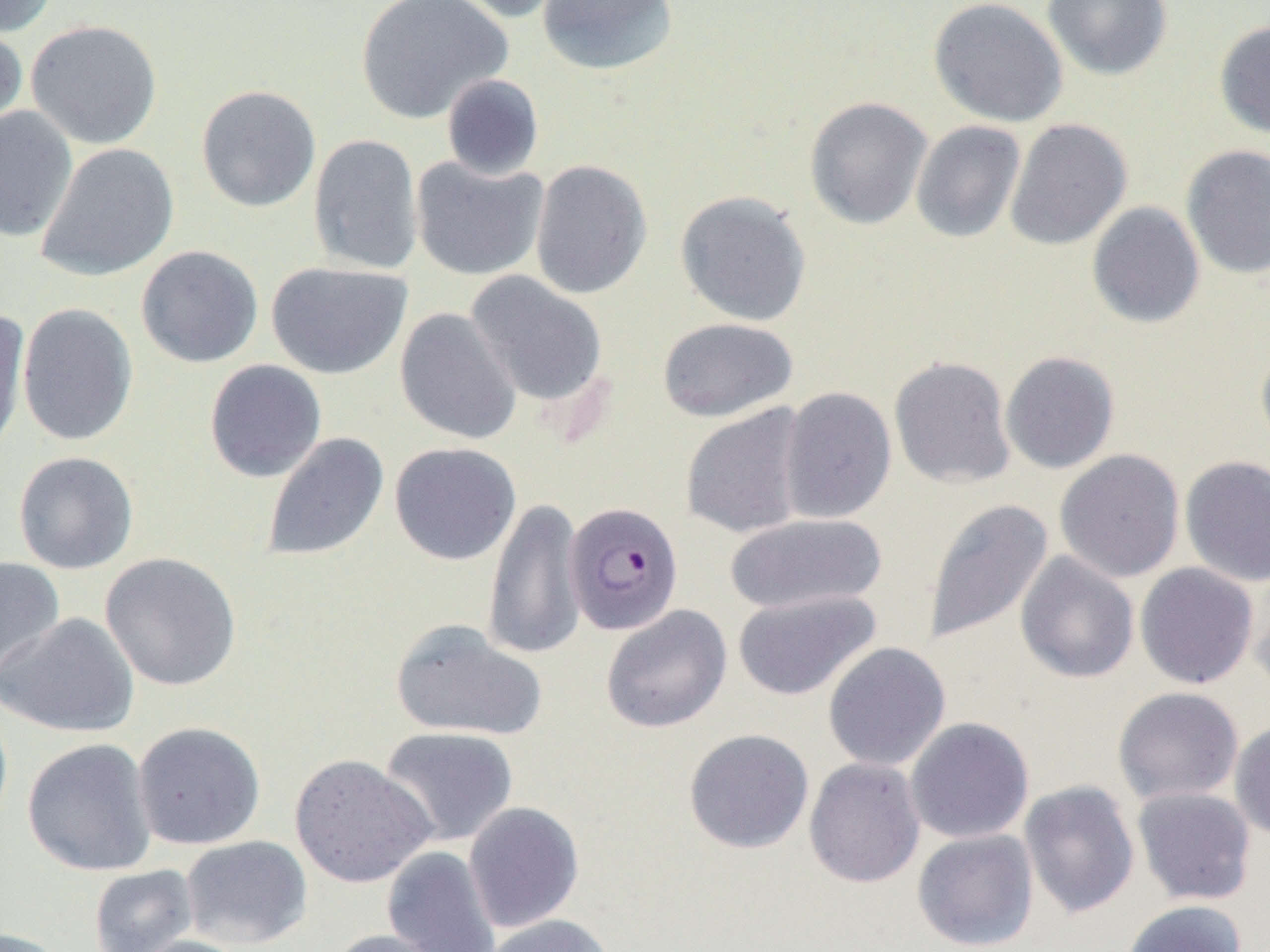

Summary:
  - Coordinate format: approximate bounding boxes as (x1,y1)-(x2,y2) corner pairs in pixels
  - Plasmodium falciparum-infected red blood cell locations: (564,501)-(683,635)
  - Uninfected red blood cell locations: (0,0)-(59,37), (353,0)-(512,124), (447,0)-(576,23), (537,0)-(679,76), (928,0)-(1068,127), (1042,0)-(1173,81), (25,19)-(163,150), (1213,20)-(1270,140), (0,22)-(28,138), (441,74)-(545,181), (195,84)-(321,212), (804,96)-(933,230), (0,106)-(79,242), (1004,118)-(1132,250), (910,120)-(1026,243), (308,134)-(423,276), (36,142)-(179,282), (1181,145)-(1270,279), (410,156)-(549,281), (529,159)-(652,300), (675,190)-(812,327), (1086,201)-(1206,329), (136,245)-(263,368), (266,261)-(412,379), (465,271)-(608,408), (17,302)-(138,446), (0,308)-(31,459), (395,308)-(522,445), (657,317)-(798,422), (1255,342)-(1270,455), (1000,351)-(1120,474), (889,356)-(1016,489), (204,359)-(327,483), (779,386)-(897,524), (681,404)-(811,539), (261,431)-(389,562), (389,442)-(521,566), (1054,449)-(1185,583), (13,451)-(138,574), (1179,455)-(1270,588), (482,496)-(587,661), (922,498)-(1055,646), (723,513)-(888,615), (1015,551)-(1140,684), (99,552)-(242,692), (0,556)-(65,686), (1134,562)-(1259,689), (1249,574)-(1270,700), (731,589)-(881,701), (601,605)-(732,733), (2,612)-(138,738), (390,619)-(547,742), (822,642)-(951,771), (1113,687)-(1244,805), (0,700)-(13,839), (905,717)-(1034,844), (1229,720)-(1270,842), (132,721)-(266,850), (379,726)-(519,847), (683,728)-(814,854), (22,738)-(157,877), (289,753)-(436,888), (804,757)-(925,888), (1018,780)-(1140,918), (1132,786)-(1257,905), (463,802)-(584,933), (912,829)-(1039,950), (180,835)-(312,949), (382,846)-(502,952), (88,864)-(199,952), (1120,900)-(1248,952), (480,914)-(617,952), (0,926)-(71,952), (324,929)-(455,952), (121,934)-(252,952)
  - Slide-level diagnosis: Plasmodium falciparum
  - Preparation: thin blood film
  - Modality: light microscopy
  - Field of view: one of a larger specimen
  - Magnification: 1000x
  - Image size: 1270×952 pixels